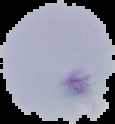

preparation = thin blood film
result = no Plasmodium parasites seen
image type = segmented cell region on a black background
image size = 115×124 pixels